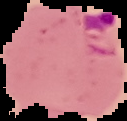
image type = segmented cell region on a black background
preparation = thin blood smear
image size = 127×121 pixels
malaria status = parasitized